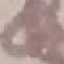

result = no malaria parasites detected
stain = Giemsa
preparation = thin smear
capture = smartphone camera at the microscope eyepiece
image type = cell patch, automatically extracted from a larger field of view and resized to 64 × 64 pixels